Identify the parasite.
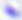

This is Toxoplasma gondii.

Summary:
  - Modality: photomicrograph
  - Magnification: 400x